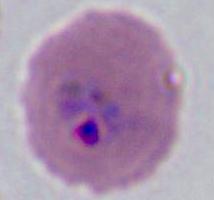
identification = Plasmodium
magnification = 400x or 1000x
modality = micrograph